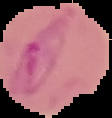
Summary:
  - Image type: cell region segmented out of the field of view; surrounding area masked to black
  - Preparation: thin blood film
  - Malaria status: parasitized
  - Image size: 112×118 pixels